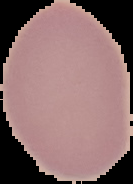

image_type: segmented cell region on a black background
preparation: thin blood film
image_size: 133×184 pixels
malaria_status: uninfected